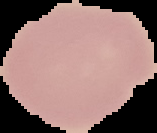
Image is 157×133 pixels. Segmented cell region on a black background. Malaria status: uninfected. From a thin blood film.